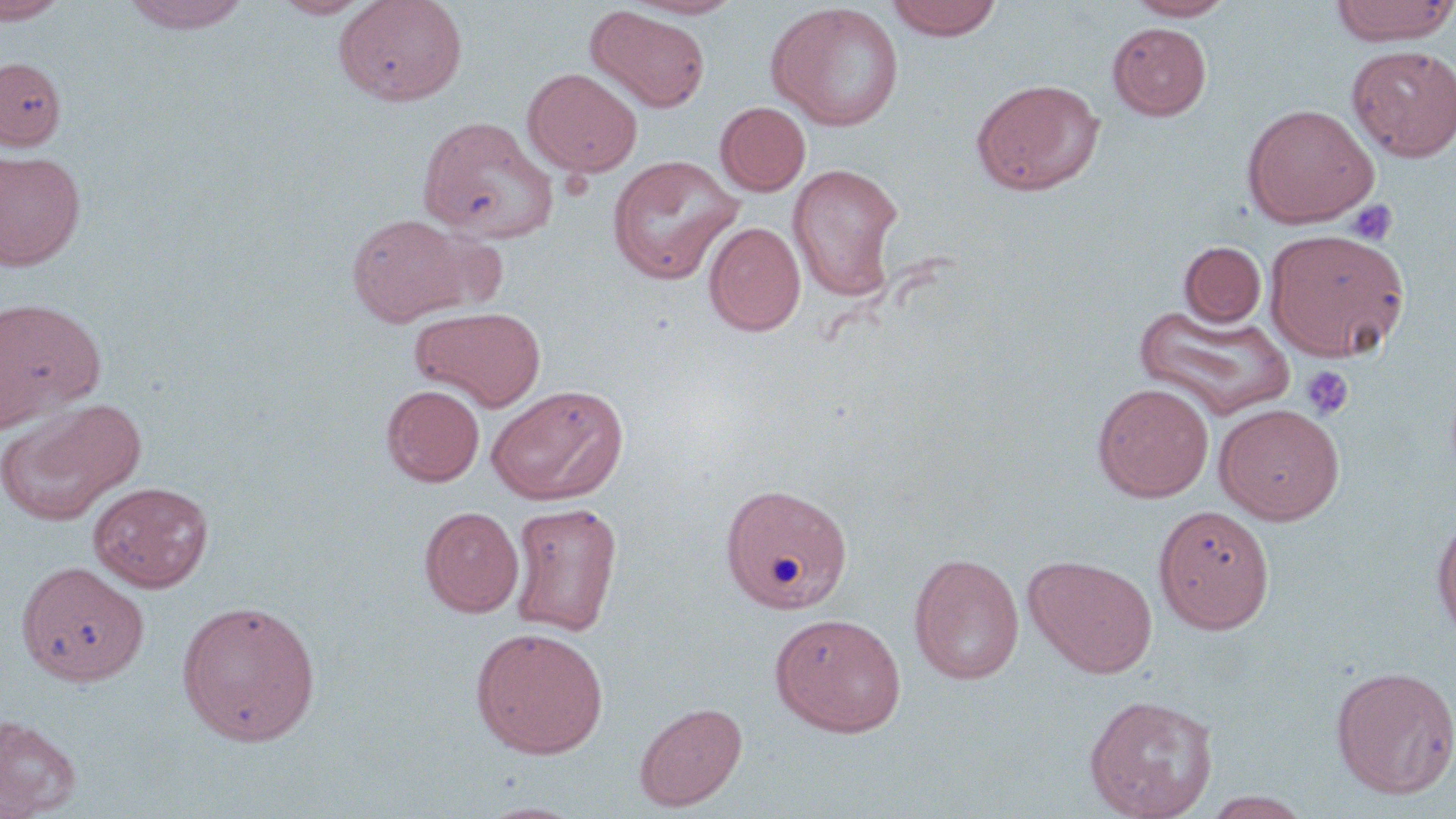 Approximate bounding boxes as named x1/y1/x2/y2 corners in pixels. Platelet locations: (x1=1347, y1=199, x2=1399, y2=246), (x1=1301, y1=365, x2=1354, y2=419). Uninfected red blood cell locations: (x1=0, y1=0, x2=69, y2=24), (x1=120, y1=0, x2=252, y2=33), (x1=270, y1=0, x2=376, y2=19), (x1=335, y1=0, x2=468, y2=106), (x1=624, y1=0, x2=746, y2=19), (x1=884, y1=0, x2=1004, y2=40), (x1=1125, y1=0, x2=1237, y2=20), (x1=1329, y1=0, x2=1456, y2=46), (x1=766, y1=3, x2=905, y2=131), (x1=586, y1=5, x2=711, y2=113), (x1=1108, y1=22, x2=1212, y2=120), (x1=1347, y1=45, x2=1456, y2=162), (x1=0, y1=57, x2=65, y2=150), (x1=522, y1=67, x2=642, y2=177), (x1=971, y1=78, x2=1104, y2=196), (x1=715, y1=101, x2=811, y2=196), (x1=1242, y1=103, x2=1379, y2=228), (x1=418, y1=115, x2=559, y2=243), (x1=0, y1=152, x2=85, y2=271), (x1=606, y1=155, x2=744, y2=285), (x1=787, y1=163, x2=905, y2=301), (x1=345, y1=213, x2=482, y2=325), (x1=703, y1=221, x2=805, y2=336), (x1=1264, y1=228, x2=1411, y2=361), (x1=1179, y1=241, x2=1266, y2=327), (x1=0, y1=296, x2=104, y2=430), (x1=1132, y1=304, x2=1296, y2=420), (x1=410, y1=305, x2=547, y2=411), (x1=486, y1=383, x2=629, y2=505), (x1=1093, y1=383, x2=1214, y2=502), (x1=381, y1=384, x2=485, y2=486), (x1=0, y1=399, x2=145, y2=526), (x1=1214, y1=403, x2=1344, y2=524), (x1=88, y1=480, x2=213, y2=592), (x1=719, y1=481, x2=853, y2=614), (x1=509, y1=502, x2=623, y2=637), (x1=1153, y1=504, x2=1275, y2=634), (x1=419, y1=506, x2=523, y2=617), (x1=1432, y1=511, x2=1456, y2=641), (x1=909, y1=552, x2=1025, y2=685), (x1=1024, y1=554, x2=1158, y2=678), (x1=17, y1=561, x2=149, y2=686), (x1=176, y1=598, x2=322, y2=746), (x1=769, y1=611, x2=907, y2=737), (x1=470, y1=626, x2=609, y2=759), (x1=1331, y1=665, x2=1456, y2=799), (x1=1083, y1=694, x2=1219, y2=819), (x1=634, y1=701, x2=747, y2=811), (x1=0, y1=714, x2=81, y2=817), (x1=1201, y1=792, x2=1314, y2=819). Slide-level diagnosis: no evidence of blood parasites. Captured at 1000x magnification. May-Grünwald-Giemsa stain. One field of a larger specimen. Image is 1456×819 pixels. Thin blood smear. Light microscopy.